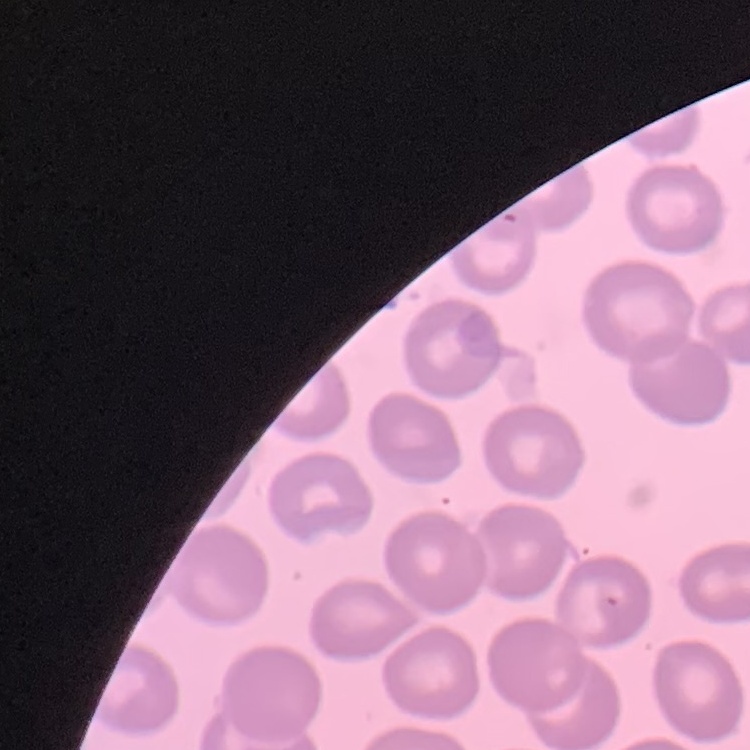

The erythrocytes show no rouleaux formation. Stained with either Field's or Giemsa. Thin peripheral smear. Square crop of a larger photomicrograph.